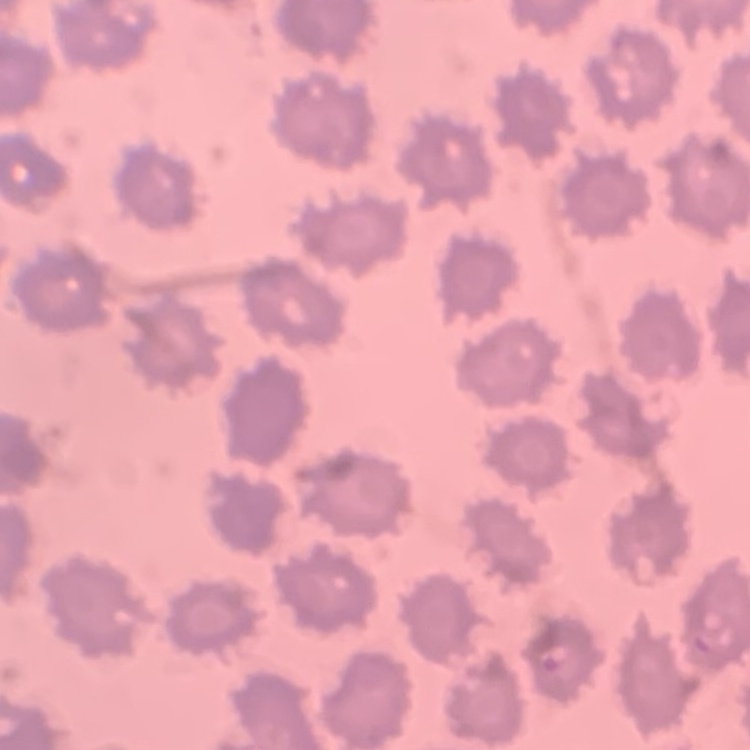

Summary:
  - Red blood cell morphology: no rouleaux formation
  - Image type: square crop of a larger photomicrograph
  - Stain: Field's or Giemsa
  - Preparation: thin blood film